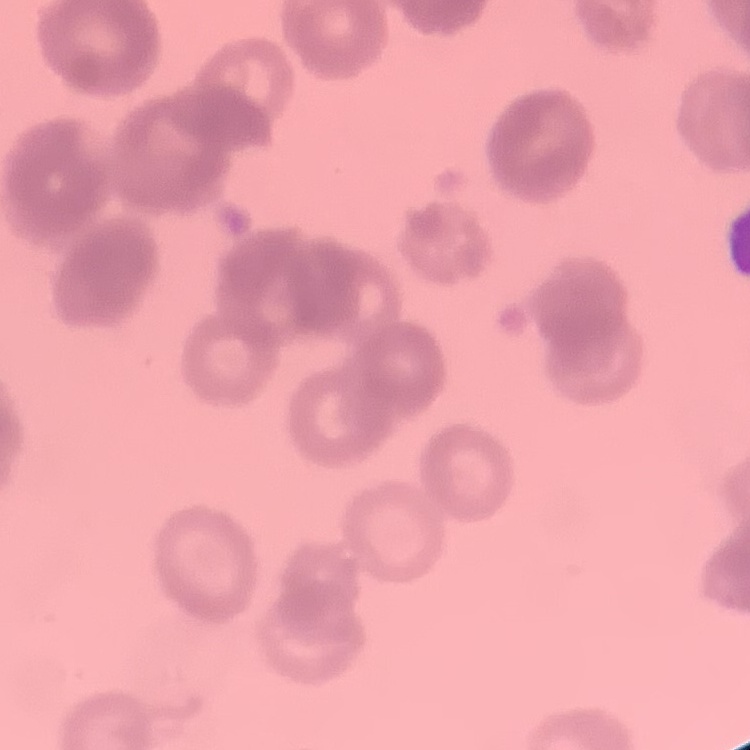

The red blood cells exhibit rouleaux formation. Square crop of a larger photomicrograph. Field's or Giemsa stain. Thin peripheral smear.